Assess this cell for malaria.
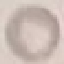
It is uninfected.

image_type: automatically extracted cell patch, resized to 64 × 64 pixels
capture: smartphone camera at the microscope eyepiece
preparation: thin blood film
stain: Giemsa